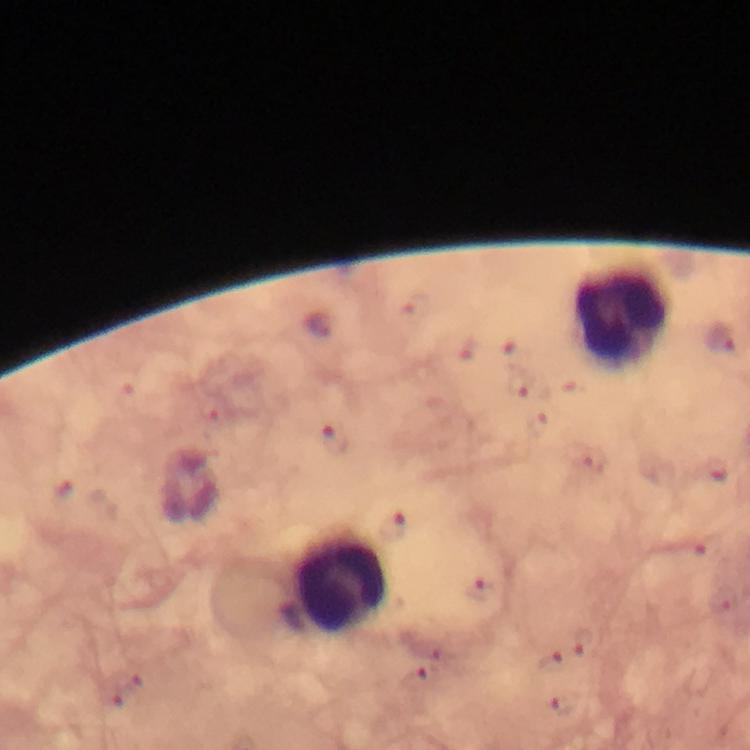

Approximate centers as [x, y] in pixels.
Summary:
  - Leukocyte locations: [622, 319], [341, 582]
  - Malaria parasite locations: [720, 335], [334, 436], [391, 528], [480, 589], [582, 642], [552, 662], [413, 681], [563, 706]
  - Magnification: 100x
  - Immersion oil: used
  - Capture: smartphone camera through the microscope
  - Cropped from: a single field of view
  - Preparation: thick blood film
  - Context: from a diagnostic examination for malaria
  - Image size: 750×750 pixels
  - Stain: Giemsa